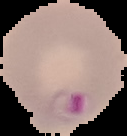

preparation = thin blood smear
image type = segmented cell region with the area outside set to black
image size = 127×136 pixels
malaria status = parasitized